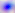

Toxoplasma gondii is seen. Photomicrograph. 400x magnification.